Give the extent of all Plasmodium falciparum-infected red blood cells.
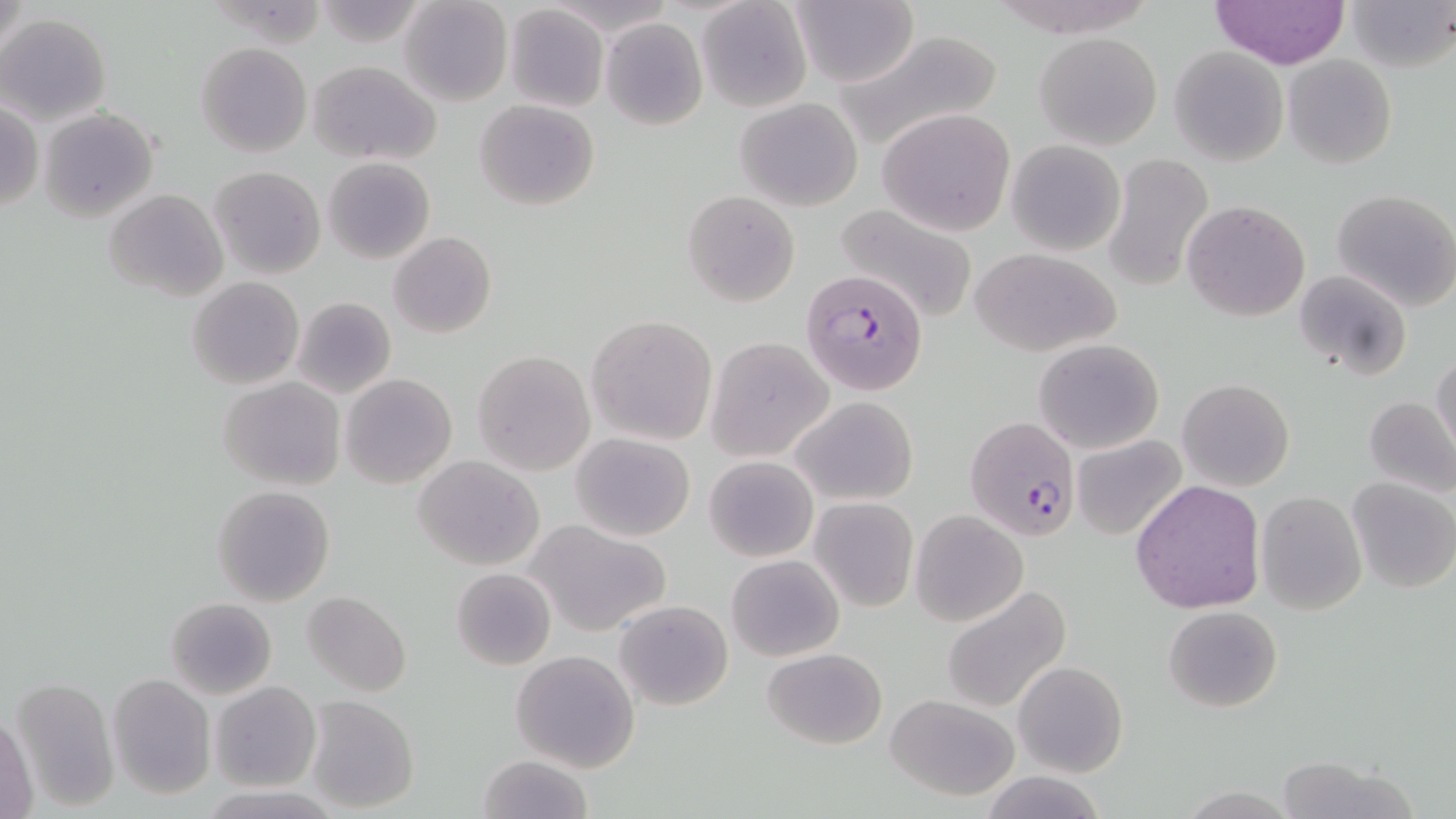

Approximate bounding boxes as named x1/y1/x2/y2 corners in pixels.
Plasmodium falciparum-infected red blood cells: (x1=799, y1=269, x2=929, y2=394), (x1=964, y1=416, x2=1083, y2=541).

{
  "slide_level_diagnosis": "Plasmodium falciparum",
  "magnification": "1000x",
  "image_size": "1456×819 pixels",
  "field_of_view": "one of a larger specimen",
  "stain": "May-Grünwald-Giemsa",
  "uninfected_red_blood_cell_locations": "approximate bounding boxes as named x1/y1/x2/y2 corners in pixels: (x1=398, y1=0, x2=514, y2=108), (x1=1210, y1=0, x2=1350, y2=69), (x1=1345, y1=0, x2=1456, y2=72), (x1=697, y1=1, x2=811, y2=111), (x1=790, y1=1, x2=919, y2=88), (x1=503, y1=4, x2=609, y2=113), (x1=1, y1=14, x2=111, y2=124), (x1=600, y1=18, x2=708, y2=131), (x1=834, y1=28, x2=1006, y2=151), (x1=1034, y1=31, x2=1163, y2=150), (x1=195, y1=42, x2=313, y2=157), (x1=1169, y1=47, x2=1288, y2=165), (x1=1283, y1=54, x2=1396, y2=168), (x1=307, y1=60, x2=441, y2=164), (x1=734, y1=97, x2=865, y2=211), (x1=474, y1=100, x2=600, y2=210), (x1=1, y1=102, x2=43, y2=213), (x1=38, y1=108, x2=157, y2=220), (x1=879, y1=109, x2=1016, y2=235), (x1=1007, y1=140, x2=1125, y2=255), (x1=1102, y1=153, x2=1215, y2=294), (x1=323, y1=157, x2=435, y2=264), (x1=210, y1=165, x2=324, y2=279), (x1=105, y1=189, x2=228, y2=302), (x1=1331, y1=189, x2=1456, y2=311), (x1=682, y1=190, x2=800, y2=307), (x1=831, y1=200, x2=982, y2=324), (x1=1182, y1=200, x2=1310, y2=320), (x1=389, y1=231, x2=496, y2=339), (x1=970, y1=247, x2=1121, y2=357), (x1=1295, y1=269, x2=1412, y2=380), (x1=188, y1=276, x2=304, y2=390), (x1=291, y1=296, x2=396, y2=400), (x1=587, y1=314, x2=717, y2=446), (x1=706, y1=336, x2=834, y2=461), (x1=1032, y1=338, x2=1165, y2=454), (x1=472, y1=350, x2=595, y2=474), (x1=1430, y1=353, x2=1456, y2=467), (x1=340, y1=374, x2=457, y2=489), (x1=218, y1=377, x2=345, y2=491), (x1=1177, y1=379, x2=1294, y2=492), (x1=1363, y1=396, x2=1456, y2=499), (x1=791, y1=397, x2=919, y2=505), (x1=572, y1=432, x2=695, y2=541), (x1=1073, y1=434, x2=1188, y2=541), (x1=415, y1=455, x2=544, y2=570), (x1=704, y1=455, x2=818, y2=562), (x1=1347, y1=477, x2=1456, y2=594), (x1=1131, y1=480, x2=1266, y2=615), (x1=211, y1=485, x2=337, y2=607), (x1=1256, y1=490, x2=1367, y2=615), (x1=809, y1=496, x2=918, y2=613), (x1=911, y1=510, x2=1028, y2=627), (x1=529, y1=520, x2=671, y2=637), (x1=726, y1=555, x2=844, y2=661), (x1=451, y1=566, x2=556, y2=670), (x1=942, y1=586, x2=1072, y2=714), (x1=302, y1=591, x2=411, y2=696), (x1=166, y1=597, x2=277, y2=699), (x1=614, y1=599, x2=734, y2=711), (x1=1164, y1=605, x2=1282, y2=712), (x1=762, y1=648, x2=887, y2=748), (x1=510, y1=651, x2=640, y2=772), (x1=1013, y1=661, x2=1128, y2=778), (x1=107, y1=673, x2=214, y2=799), (x1=10, y1=678, x2=119, y2=812), (x1=210, y1=681, x2=322, y2=791), (x1=886, y1=693, x2=1022, y2=802), (x1=302, y1=696, x2=420, y2=814), (x1=1, y1=709, x2=38, y2=819), (x1=475, y1=754, x2=591, y2=819), (x1=1274, y1=757, x2=1416, y2=818), (x1=984, y1=772, x2=1105, y2=818), (x1=200, y1=785, x2=340, y2=818)",
  "modality": "optical microscopy",
  "preparation": "thin blood smear"
}